Locate every malaria parasite and every leukocyte.
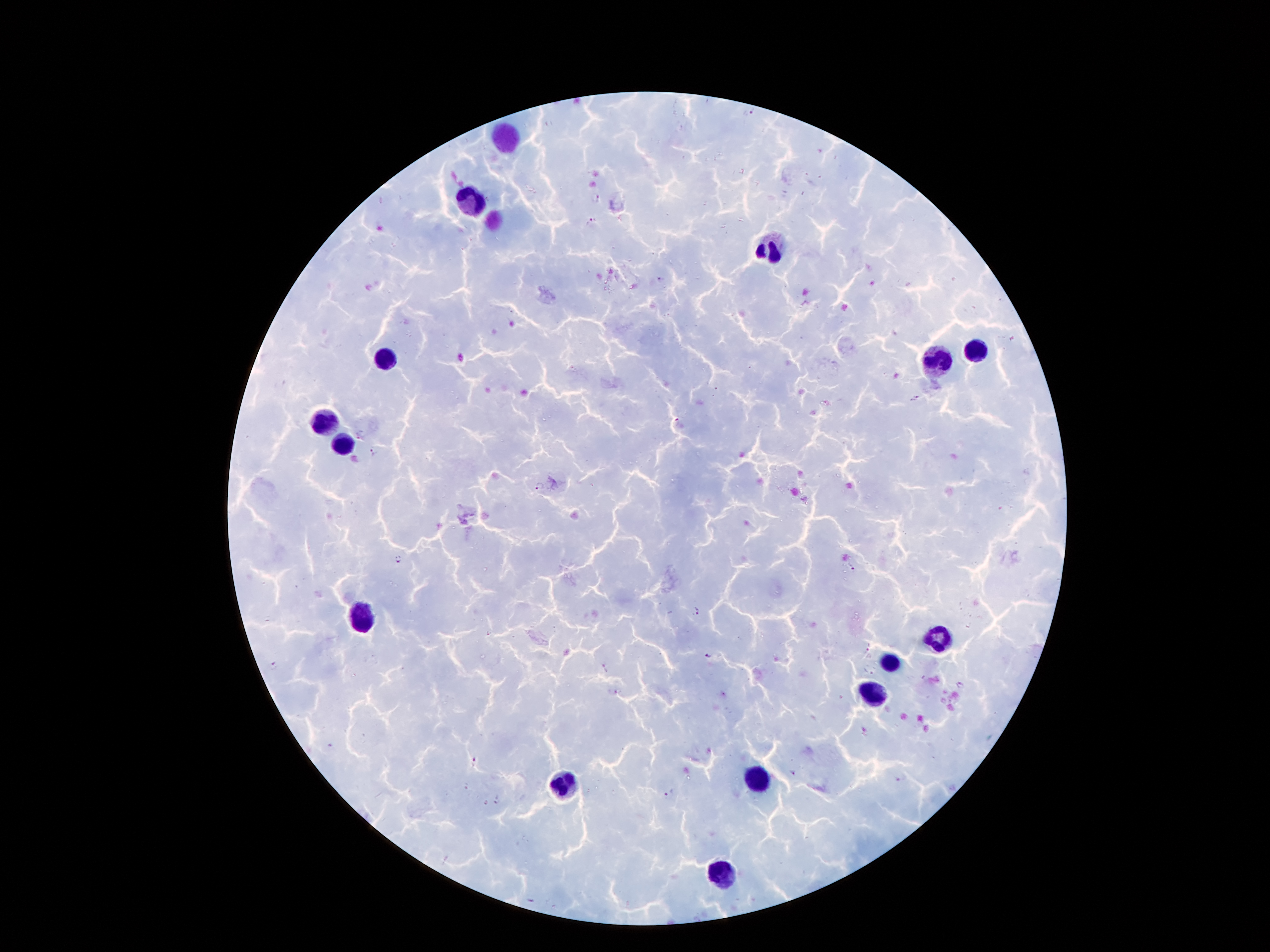

Approximate centers as (x, y) in pixels.
Malaria parasites: (750, 111), (596, 196), (591, 222), (659, 280), (915, 397), (676, 422), (360, 433), (374, 452), (539, 487), (398, 559), (852, 569), (698, 611), (710, 654), (274, 667), (604, 668), (613, 692), (475, 763), (791, 773), (901, 778), (669, 792).
Leukocytes: (473, 199), (768, 250), (975, 352), (382, 359), (936, 364), (324, 422), (341, 444), (362, 619), (938, 640), (889, 661), (877, 694), (756, 777), (569, 782), (721, 875).

{
  "magnification": "100x",
  "patient_malaria_status": "infected with Plasmodium falciparum",
  "image_size": "1270×952 pixels",
  "stain": "Giemsa",
  "preparation": "thick peripheral-blood smear",
  "field_of_view": "single",
  "capture": "smartphone through the microscope eyepiece"
}